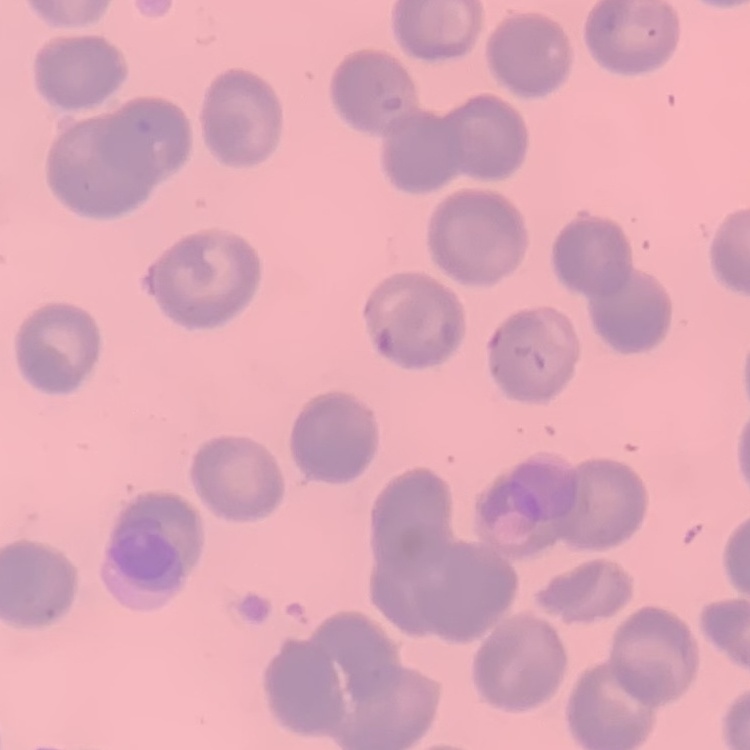

Summary:
  - Red blood cell morphology: no rouleaux formation
  - Preparation: thin blood film
  - Image type: one tile cut from a larger photomicrograph
  - Stain: Field's or Giemsa